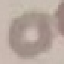

Summary:
  - Malaria status: uninfected
  - Capture: smartphone through the microscope eyepiece
  - Preparation: thin blood film
  - Stain: Giemsa
  - Image type: cell patch, automatically extracted from a larger field of view and resized to 64 × 64 pixels